Report the malaria status of this cell.
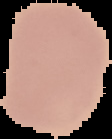

It is uninfected.

image type = segmented cell region on a black background
preparation = thin blood film
image size = 112×139 pixels